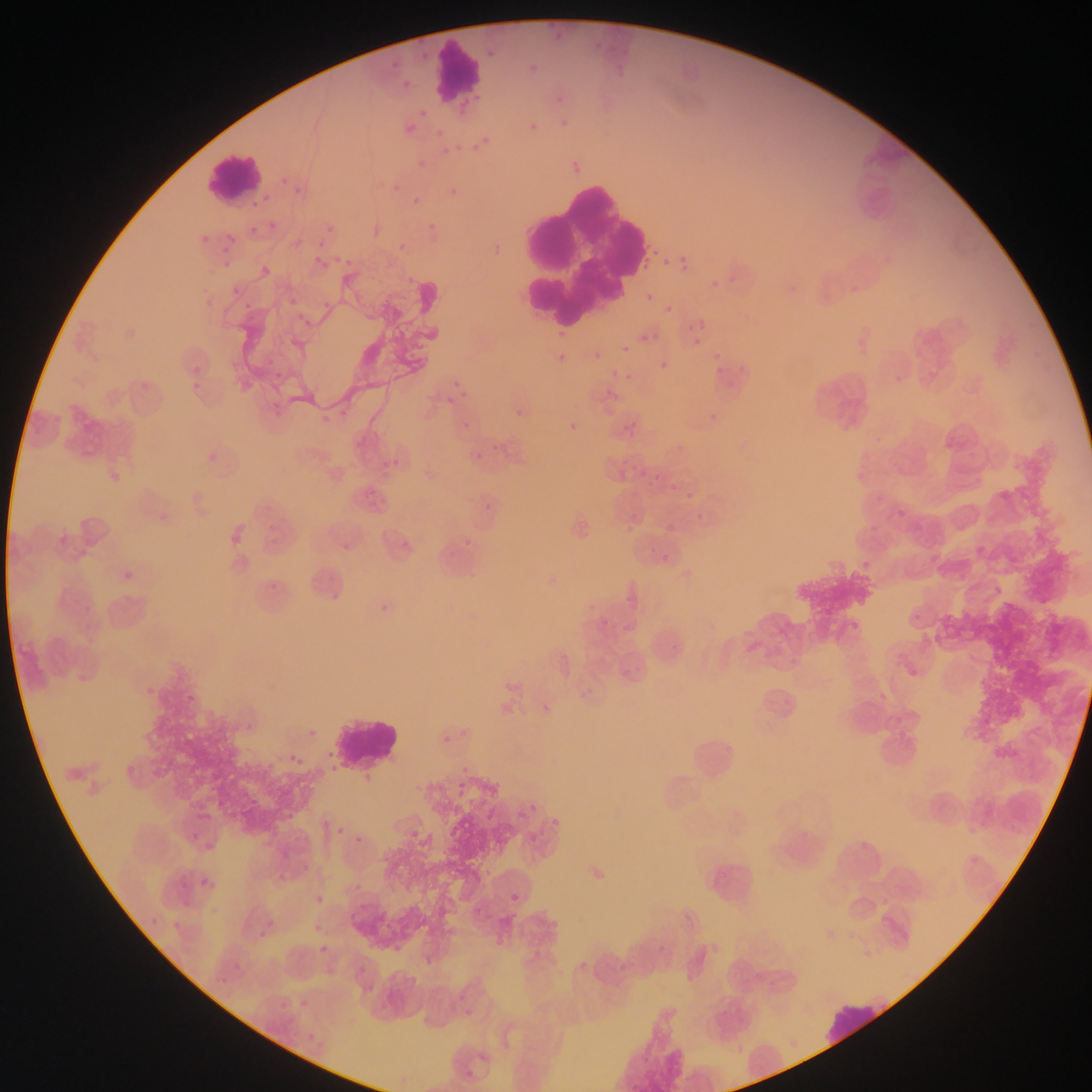

Approximate bounding boxes as [left, top, right, bottom] in pixels. Leukocyte locations: [429, 39, 484, 100], [205, 149, 263, 205], [507, 167, 654, 332], [330, 712, 402, 769], [685, 726, 744, 792], [821, 995, 890, 1050]. Plasmodium parasite locations: [485, 47, 500, 62], [525, 59, 543, 79], [399, 77, 415, 93], [416, 106, 431, 121], [554, 114, 575, 136], [524, 119, 544, 139], [402, 121, 420, 138], [432, 124, 447, 140], [469, 134, 493, 155], [438, 144, 454, 159], [415, 158, 432, 175], [286, 177, 309, 199], [388, 179, 404, 195], [444, 181, 463, 201], [409, 193, 424, 209], [423, 219, 440, 236], [324, 222, 338, 237], [246, 223, 261, 238], [200, 224, 209, 241], [222, 230, 240, 249], [396, 239, 408, 250], [310, 252, 331, 272], [675, 254, 693, 275], [336, 255, 355, 271], [661, 258, 672, 269], [219, 260, 228, 270], [402, 269, 418, 290], [842, 273, 862, 296], [707, 276, 723, 293], [229, 283, 245, 299], [782, 285, 799, 295], [285, 292, 302, 312], [644, 292, 657, 304], [240, 297, 257, 314], [662, 302, 675, 316], [851, 326, 871, 347], [639, 331, 655, 345], [690, 336, 704, 349], [617, 342, 640, 356], [620, 344, 631, 356], [553, 346, 574, 370], [589, 349, 603, 365], [710, 349, 724, 364], [187, 354, 209, 377], [657, 360, 672, 376], [187, 370, 206, 393], [621, 370, 635, 384], [449, 376, 472, 402], [318, 400, 335, 423], [509, 403, 534, 426], [702, 406, 719, 425], [459, 414, 471, 428], [563, 417, 585, 439], [620, 417, 635, 433], [492, 435, 509, 457], [669, 438, 686, 448], [470, 448, 487, 465], [386, 454, 406, 474], [635, 469, 644, 480], [851, 471, 863, 485], [666, 479, 683, 496], [478, 492, 500, 512], [686, 496, 699, 504], [893, 505, 906, 523], [663, 513, 679, 533], [226, 521, 252, 551], [461, 529, 477, 548], [337, 533, 354, 553], [658, 548, 672, 562], [858, 556, 876, 572], [118, 568, 141, 584], [375, 598, 395, 618], [846, 617, 862, 633], [536, 705, 550, 722], [246, 718, 257, 734], [305, 722, 316, 740], [437, 728, 458, 750], [286, 742, 309, 772], [357, 770, 368, 784], [454, 775, 466, 792], [524, 794, 542, 813], [352, 815, 365, 858], [549, 820, 560, 832], [332, 823, 347, 840], [525, 830, 542, 844], [187, 831, 199, 845], [202, 847, 217, 857], [196, 874, 214, 892], [312, 886, 326, 910], [506, 890, 524, 908], [145, 914, 161, 929], [170, 919, 180, 935], [310, 924, 322, 935], [255, 928, 271, 939], [318, 943, 332, 952], [389, 943, 405, 961], [426, 955, 442, 966], [234, 964, 245, 970], [217, 973, 233, 990], [293, 996, 308, 1010], [303, 1032, 314, 1040]. Sample from Ghana. Mobile-phone photograph taken through the microscope. Image is 1092×1092 pixels. One field of view. Thin blood film.